Assess the morphology of the red blood cells.
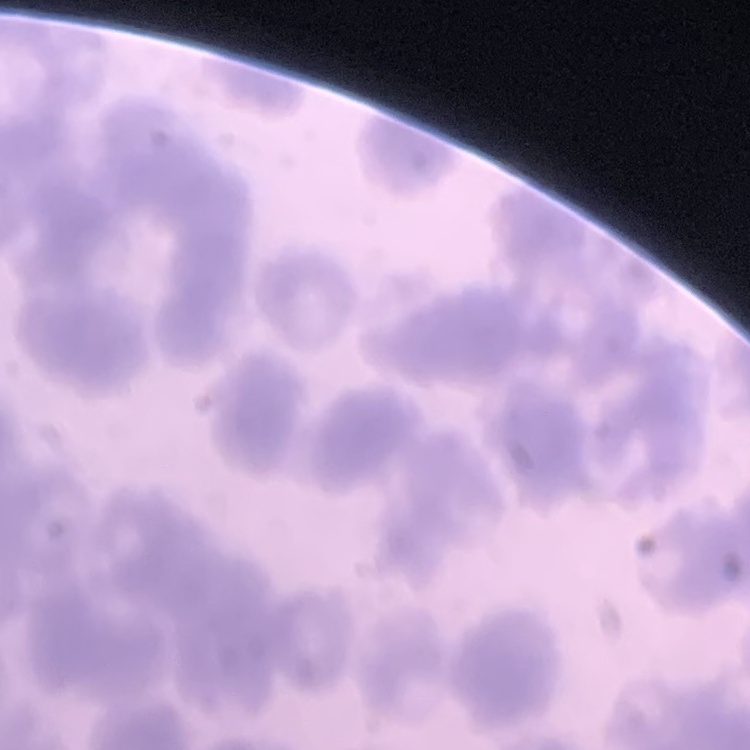
Rouleaux formation.

One tile cut from a larger photomicrograph. Stained with either Field's or Giemsa. Thin blood film.